Give the extent of all uninfected red blood cells.
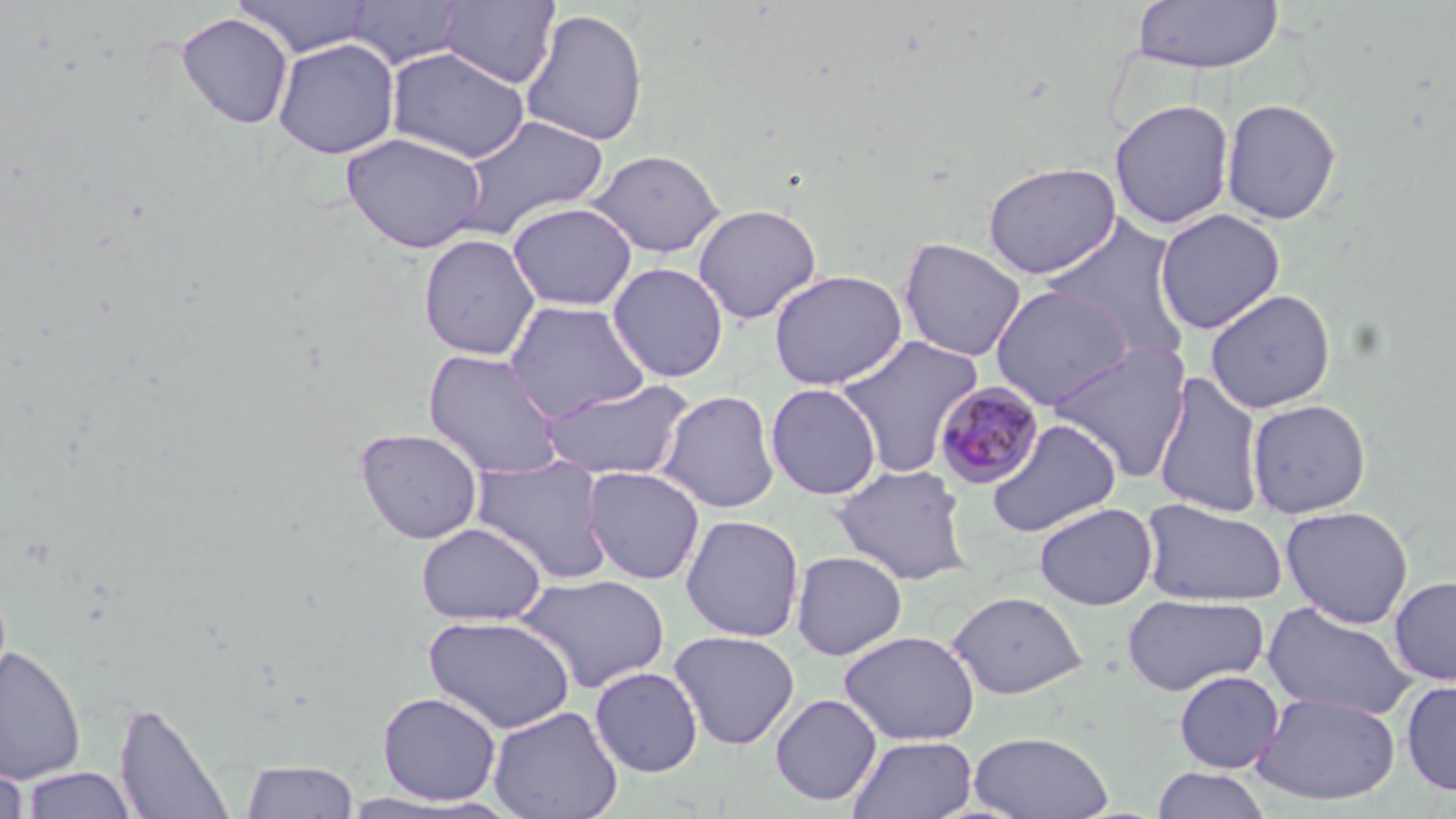

Approximate bounding boxes as (x1,y1)-(x2,y2) corner pairs in pixels.
Uninfected red blood cells: (232,0)-(376,58), (344,1)-(465,70), (438,1)-(561,88), (1132,1)-(1284,74), (520,8)-(649,147), (176,13)-(293,129), (273,38)-(400,159), (386,46)-(530,163), (1220,97)-(1342,224), (1109,99)-(1235,230), (451,114)-(609,240), (341,132)-(487,253), (589,149)-(725,258), (983,161)-(1121,279), (507,202)-(637,311), (693,204)-(822,324), (1154,208)-(1286,335), (1041,214)-(1193,364), (418,234)-(540,360), (898,238)-(1026,362), (607,262)-(729,383), (768,269)-(908,390), (990,283)-(1134,409), (1204,288)-(1336,413), (504,300)-(649,421), (834,334)-(983,475), (1048,342)-(1194,481), (422,349)-(566,479), (1152,370)-(1266,518), (539,377)-(693,481), (765,383)-(882,500), (657,388)-(780,513), (1246,398)-(1372,518), (986,418)-(1122,537), (354,427)-(484,544), (472,455)-(612,583), (831,463)-(974,584), (581,465)-(705,585), (1139,497)-(1289,607), (1034,502)-(1158,610), (1280,505)-(1414,628), (680,514)-(805,642), (416,522)-(546,625), (791,550)-(908,660), (515,573)-(671,693), (1388,576)-(1456,686), (946,590)-(1088,699), (1121,593)-(1268,696), (1260,601)-(1418,721), (423,615)-(576,734), (668,630)-(801,750), (838,630)-(980,745), (0,644)-(86,785), (590,667)-(703,777), (1173,670)-(1284,774), (1400,678)-(1456,796), (1251,690)-(1402,806), (377,691)-(502,806), (770,693)-(882,806), (114,700)-(236,819), (488,705)-(622,819), (968,730)-(1114,818), (848,734)-(978,819), (0,756)-(30,819), (239,759)-(360,818), (22,767)-(137,818), (1151,767)-(1272,819).

Summary:
  - Plasmodium malariae-infected red blood cell locations: (933,381)-(1045,490)
  - Slide-level diagnosis: Plasmodium malariae
  - Stain: May-Grünwald-Giemsa
  - Modality: light microscopy
  - Field of view: one of a larger specimen
  - Preparation: thin blood film
  - Image size: 1456×819 pixels
  - Magnification: 1000x